Name the blood parasite species.
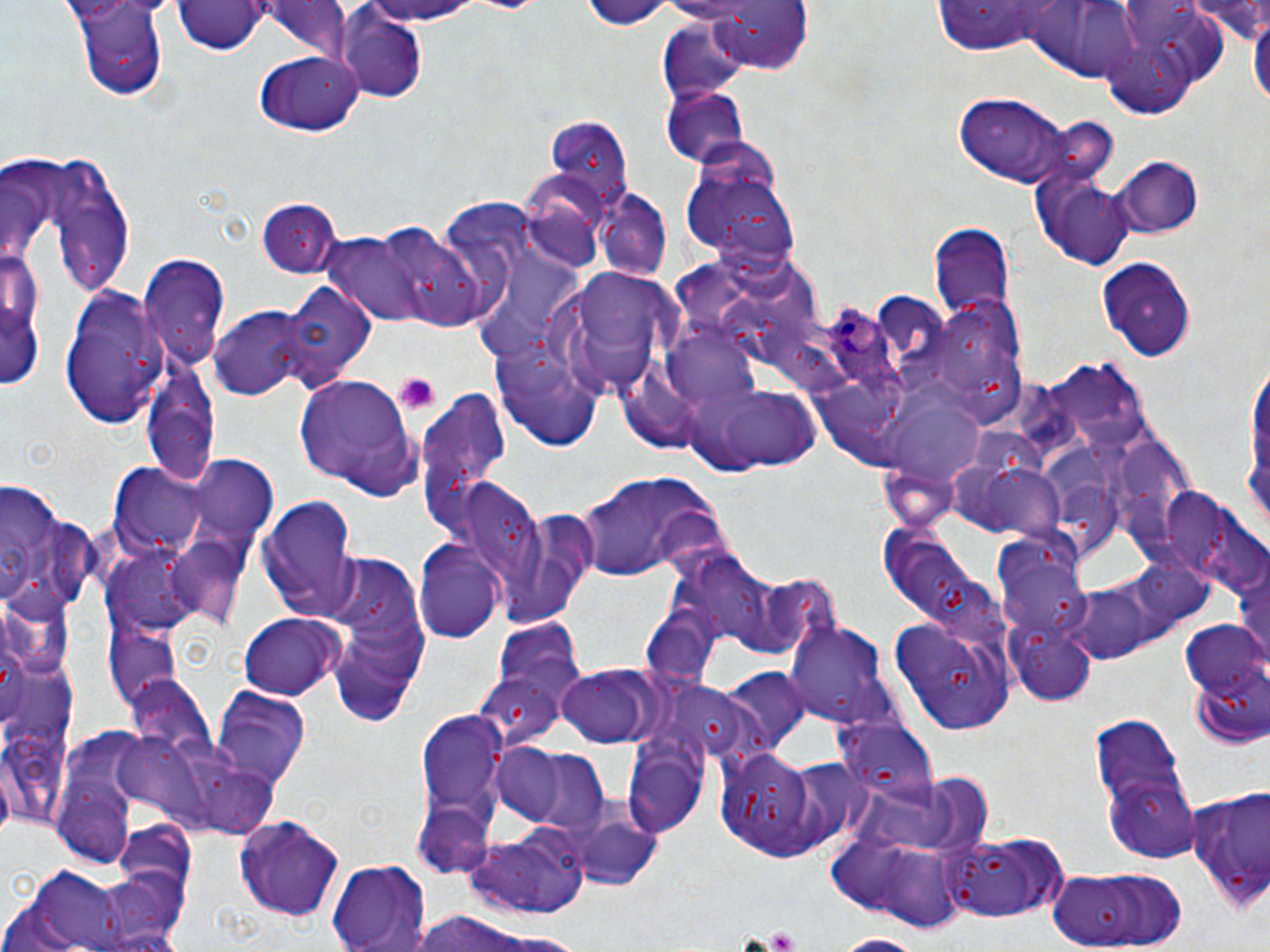
Plasmodium ovale.

Summary:
  - Coordinate format: approximate bounding boxes as (x1,y1)-(x2,y2) corner pairs in pixels
  - Uninfected red blood cell locations: (349,0)-(490,26), (453,0)-(550,15), (580,0)-(675,29), (698,0)-(815,75), (73,1)-(171,102), (1186,1)-(1268,43), (175,2)-(267,56), (258,4)-(360,58), (1032,4)-(1147,80), (1250,7)-(1270,114), (338,13)-(427,101), (658,19)-(753,102), (1099,24)-(1209,116), (255,50)-(363,135), (662,88)-(748,167), (953,92)-(1076,188), (1053,110)-(1113,182), (544,115)-(635,217), (680,145)-(798,268), (15,155)-(139,299), (1116,158)-(1200,237), (1041,176)-(1136,269), (593,189)-(672,280), (253,197)-(339,274), (358,224)-(493,330), (930,225)-(1015,322), (1,239)-(45,388), (503,244)-(586,333), (1098,253)-(1200,360), (140,256)-(229,371), (548,269)-(682,398), (277,282)-(376,394), (56,284)-(167,429), (208,304)-(311,402), (932,307)-(1004,399), (492,343)-(603,452), (140,354)-(220,489), (1053,363)-(1149,448), (292,375)-(423,496), (685,377)-(824,475), (418,390)-(511,539), (887,403)-(984,491), (186,457)-(279,548), (984,460)-(1076,549), (111,464)-(207,556), (578,473)-(710,580), (0,482)-(94,622), (458,483)-(546,584), (1161,487)-(1265,598), (258,495)-(361,620), (490,503)-(600,629), (168,538)-(253,630), (415,538)-(505,647), (318,554)-(431,711), (683,554)-(769,645), (1232,558)-(1270,666), (999,567)-(1094,635), (0,590)-(76,677), (236,612)-(346,700), (887,615)-(1013,738), (1178,616)-(1269,743), (786,619)-(890,730), (1018,637)-(1099,706), (556,665)-(660,749), (721,669)-(815,757), (472,672)-(561,748), (123,676)-(217,766), (212,686)-(311,789), (416,703)-(511,845), (1093,711)-(1199,858), (850,722)-(941,814), (49,732)-(148,865), (489,743)-(573,827), (623,744)-(705,840), (716,745)-(843,861), (520,748)-(610,840), (1185,783)-(1267,911), (573,810)-(663,892), (233,813)-(346,921), (114,817)-(196,896), (460,827)-(591,914), (943,830)-(1066,922), (837,841)-(968,930), (325,858)-(432,952), (6,861)-(143,951), (1043,864)-(1188,951), (85,867)-(190,952), (409,907)-(561,952), (827,934)-(933,951)
  - Plasmodium ovale-infected red blood cell locations: (825,300)-(910,399)
  - Platelet locations: (394,372)-(440,415), (766,925)-(800,952)
  - Stain: May-Grünwald-Giemsa
  - Magnification: 1000x
  - Preparation: thin blood smear
  - Modality: optical microscopy
  - Image size: 1270×952 pixels
  - Field of view: single